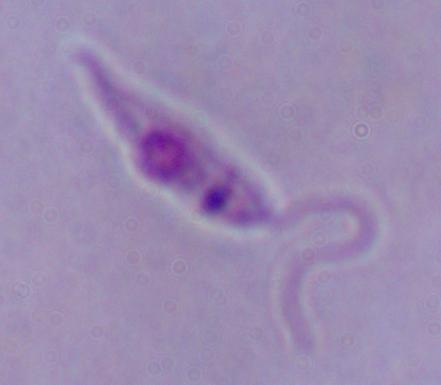 1000x magnification. A Leishmania parasite is shown. Photomicrograph.